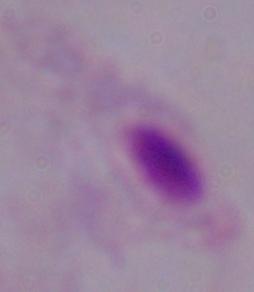 Micrograph. 1000x magnification. A trichomonad is shown.